Identify the parasite.
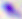

This is Toxoplasma gondii.

Micrograph. Captured at 400x magnification.